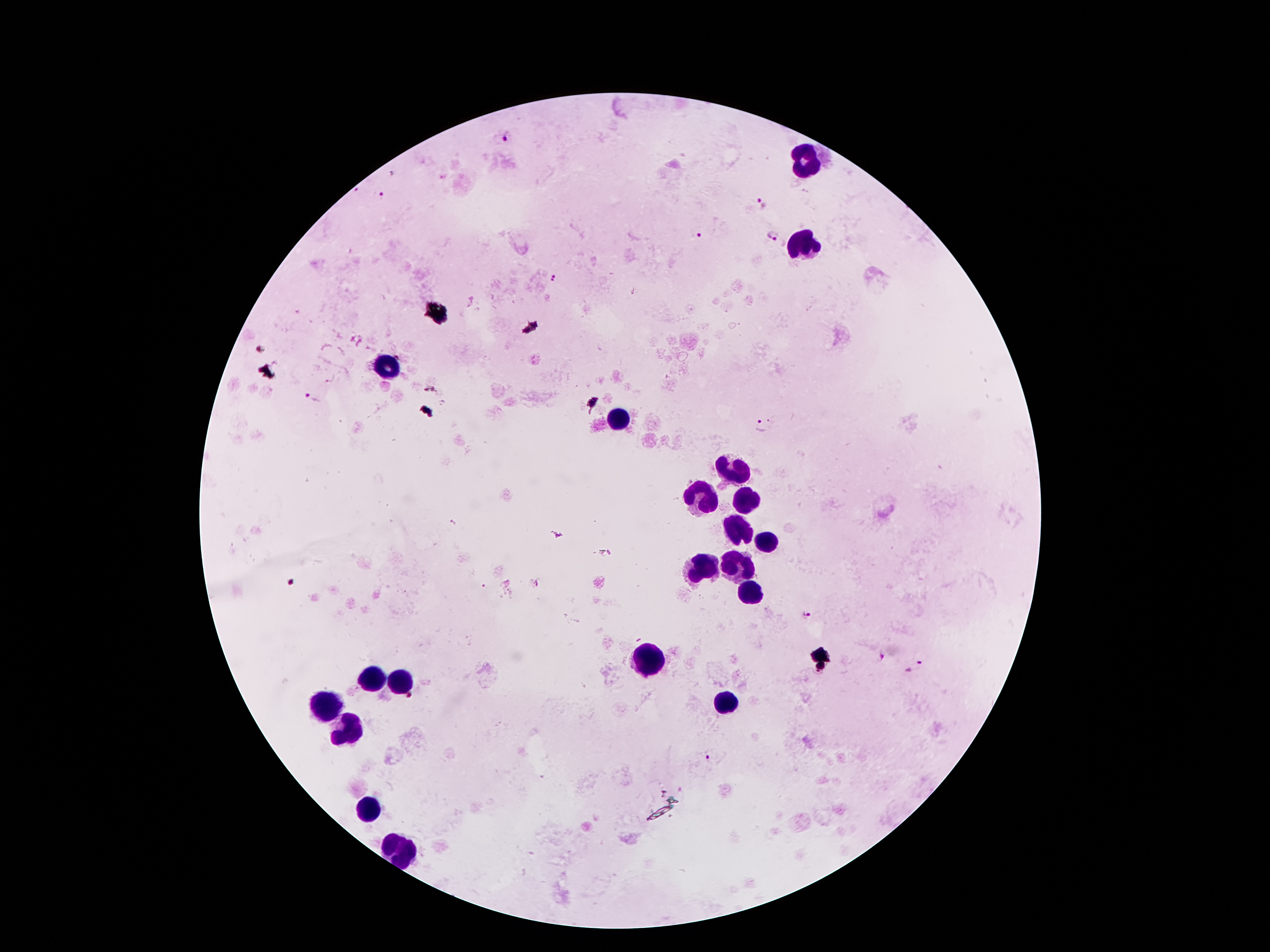
Approximate centers as [x, y] in pixels. Leukocyte locations: [805, 162], [801, 247], [391, 366], [622, 421], [734, 472], [699, 491], [746, 498], [735, 531], [767, 545], [730, 566], [698, 572], [754, 594], [650, 659], [376, 677], [401, 677], [333, 700], [729, 702], [342, 729], [376, 807], [401, 852]. Malaria parasite locations: [508, 137], [382, 196], [759, 203], [701, 236], [772, 236], [554, 279], [311, 400], [761, 425], [806, 615], [879, 659], [915, 665], [709, 757]. Single field of view. Photographed through the microscope eyepiece with a smartphone camera. 100x magnification. Giemsa stain. Image is 1270×952 pixels. Thick blood film. Patient malaria status: infected with Plasmodium falciparum.